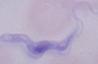

Captured at 1000x magnification. Photomicrograph. A trypanosome is seen.